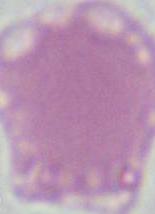
Micrograph. Captured at 1000x magnification. A red blood cell is seen.